Classify this cell by malaria status.
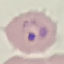

Parasitized.

Summary:
  - Capture: smartphone through the microscope eyepiece
  - Image type: automatically extracted cell patch, resized to 64 × 64 pixels
  - Stain: Giemsa
  - Preparation: thin blood film